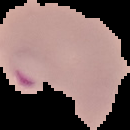
Image is 130×130 pixels. The area outside the segmented cell region is set to black. From a thin blood smear. Malaria status: parasitized.